Report the malaria status of this cell.
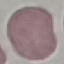
Uninfected.

Summary:
  - Stain: Giemsa
  - Preparation: thin blood film
  - Capture: smartphone through the microscope eyepiece
  - Image type: automatically extracted cell patch, resized to 64 × 64 pixels